Classify this cell by malaria status.
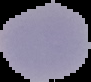

It is parasitized.

Image is 91×82 pixels. From a thin blood smear. The area outside the segmented cell region is set to black.